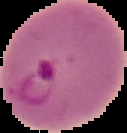
Summary:
  - Preparation: thin blood film
  - Image type: segmented cell region with the area outside set to black
  - Image size: 127×133 pixels
  - Result: malaria parasites identified